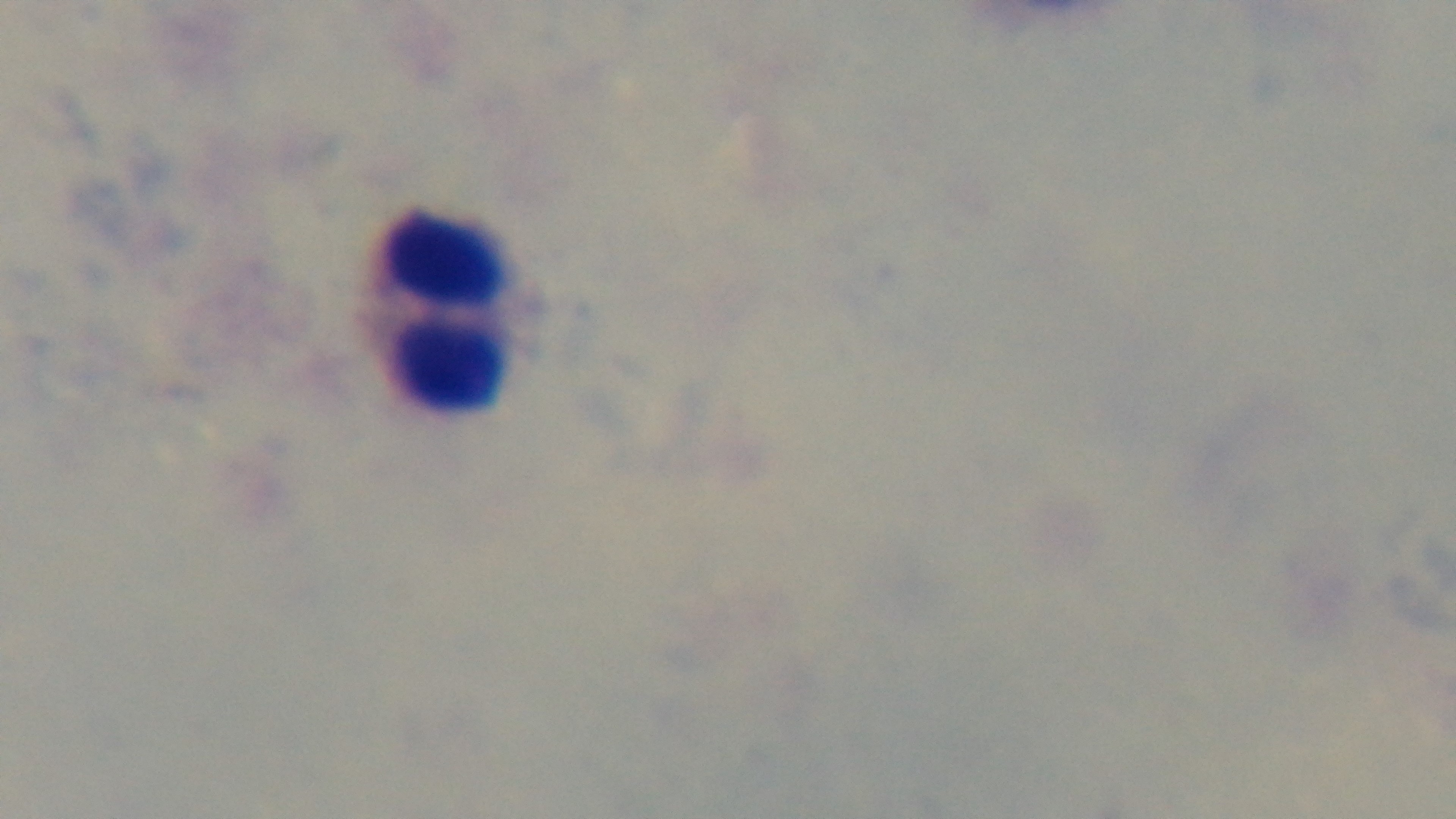
Mounted 4K digital camera. Preparation: thick blood film. 100x oil-immersion objective. Giemsa stain. Light microscopy. Malaria status: negative. One field from the slide.